Locate every Plasmodium falciparum-infected red blood cell.
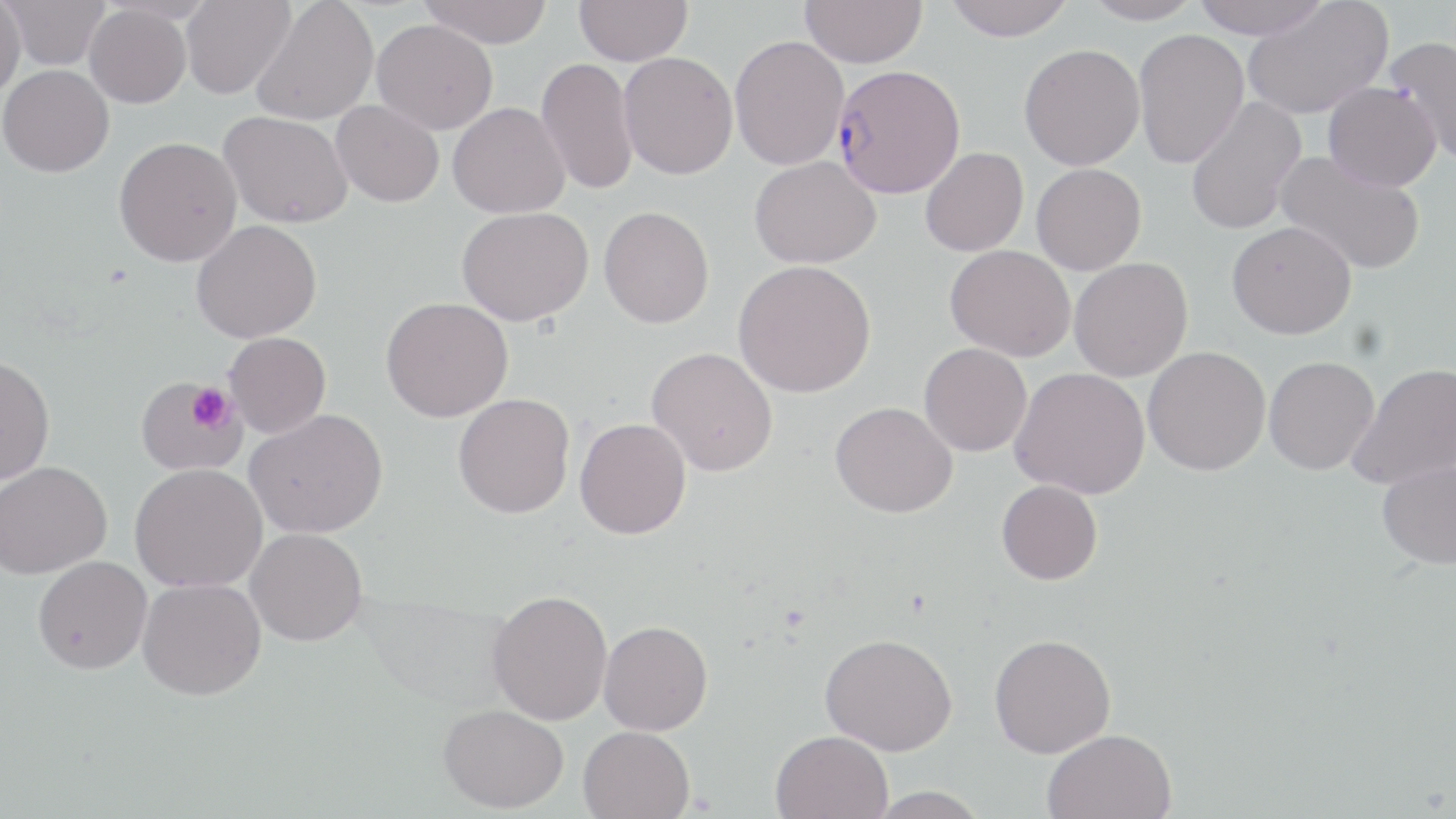

Approximate bounding boxes as (x1, y1, x2, y2) in pixels.
Plasmodium falciparum-infected red blood cells: (833, 64, 965, 198).

Summary:
  - Uninfected red blood cell locations: (3, 0, 111, 70), (181, 0, 295, 100), (418, 0, 554, 48), (575, 0, 691, 66), (942, 0, 1077, 40), (1082, 0, 1202, 25), (1191, 0, 1331, 39), (0, 1, 25, 100), (250, 1, 379, 126), (800, 1, 927, 67), (1242, 2, 1393, 120), (84, 5, 192, 108), (371, 18, 498, 134), (1133, 29, 1249, 169), (729, 35, 849, 170), (1384, 35, 1456, 166), (1019, 43, 1144, 170), (618, 52, 738, 179), (536, 57, 639, 196), (0, 65, 114, 177), (1323, 80, 1441, 191), (1185, 96, 1307, 235), (331, 100, 444, 207), (447, 102, 570, 218), (217, 110, 353, 228), (113, 136, 242, 267), (920, 147, 1028, 257), (1274, 150, 1425, 276), (749, 156, 880, 269), (1031, 163, 1146, 275), (598, 206, 714, 328), (455, 207, 593, 326), (190, 219, 322, 343), (1226, 221, 1356, 339), (945, 245, 1075, 361), (1069, 257, 1193, 381), (733, 260, 876, 398), (380, 297, 513, 422), (223, 332, 331, 439), (918, 343, 1032, 456), (646, 346, 778, 476), (1142, 346, 1271, 476), (0, 355, 55, 486), (1263, 356, 1379, 475), (1348, 362, 1456, 490), (1010, 367, 1150, 499), (132, 374, 250, 477), (452, 393, 574, 518), (830, 401, 957, 518), (245, 408, 388, 538), (574, 417, 691, 539), (1377, 460, 1456, 569), (0, 461, 112, 579), (129, 463, 267, 592), (996, 480, 1103, 585), (245, 528, 367, 646), (33, 556, 151, 674), (137, 577, 266, 700), (488, 589, 613, 725), (599, 620, 713, 735), (819, 632, 957, 755), (989, 634, 1116, 758), (438, 703, 568, 813), (578, 725, 695, 819), (1042, 728, 1177, 819), (770, 730, 893, 819), (865, 786, 992, 819)
  - Platelet locations: (187, 383, 234, 431)
  - Slide-level diagnosis: Plasmodium falciparum
  - Preparation: thin blood smear
  - Image size: 1456×819 pixels
  - Field of view: single
  - Magnification: 1000x
  - Stain: May-Grünwald-Giemsa
  - Modality: optical microscopy